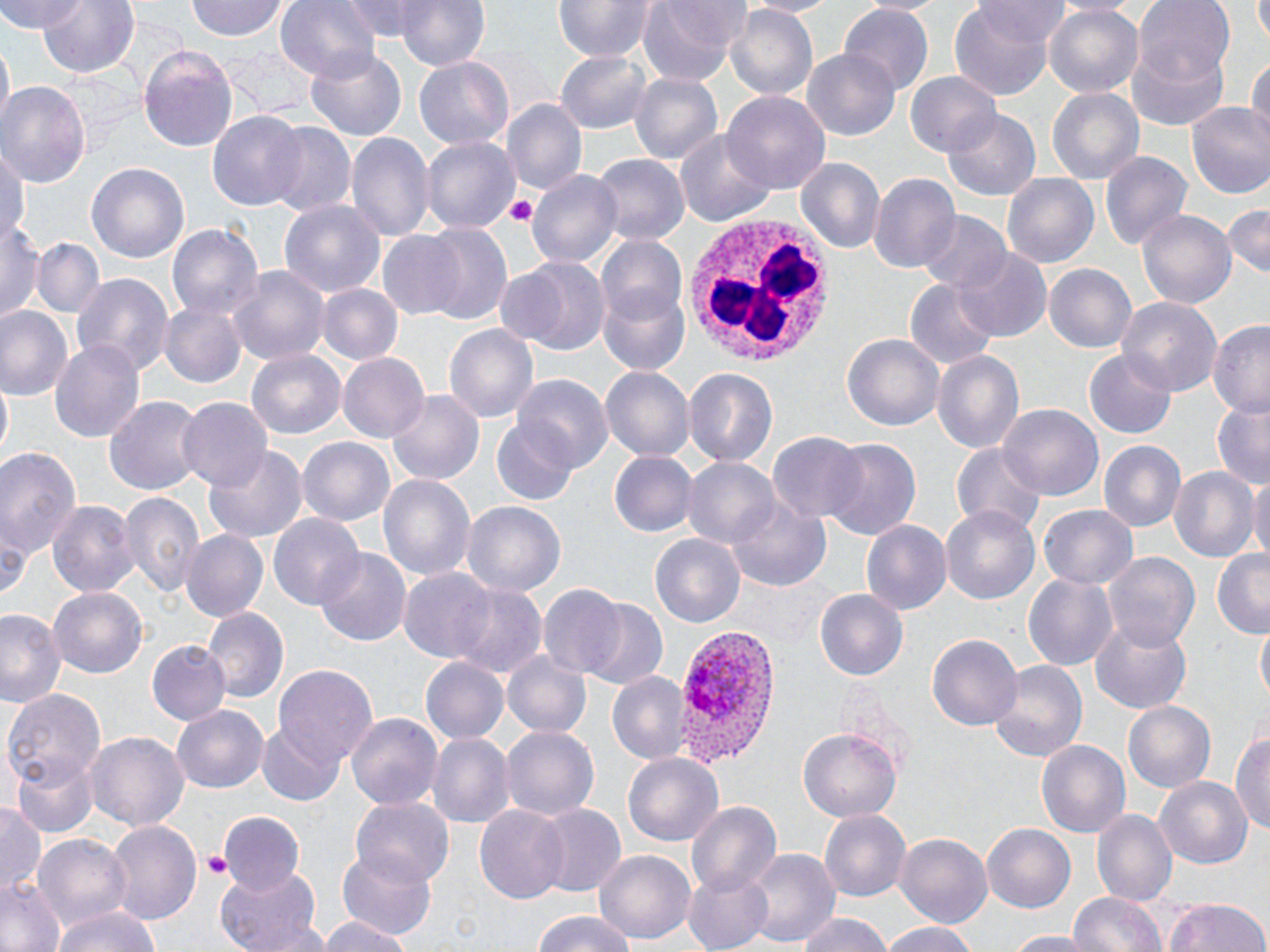

Summary:
  - Coordinate format: approximate bounding boxes as (x1,y1)-(x2,y2) corner pairs in pixels
  - Plasmodium vivax-infected red blood cell locations: (676,625)-(781,766)
  - White blood cell locations: (678,211)-(835,368)
  - Platelet locations: (501,194)-(539,225), (202,850)-(231,880)
  - Uninfected red blood cell locations: (3,0)-(82,34), (35,0)-(140,79), (186,0)-(289,41), (277,0)-(382,84), (341,0)-(436,39), (639,0)-(744,86), (742,0)-(839,18), (857,0)-(947,18), (971,0)-(1070,44), (1135,0)-(1235,87), (1254,0)-(1270,44), (390,1)-(492,69), (552,1)-(651,62), (1043,2)-(1145,99), (949,4)-(1060,99), (725,6)-(816,102), (841,7)-(933,93), (2,41)-(12,126), (1124,42)-(1230,130), (305,47)-(406,143), (555,48)-(654,136), (139,49)-(242,152), (800,50)-(901,141), (1249,56)-(1270,145), (415,57)-(514,152), (905,71)-(999,157), (629,72)-(722,169), (0,82)-(89,190), (1047,87)-(1145,187), (724,92)-(828,192), (503,99)-(586,199), (1185,102)-(1270,202), (208,110)-(310,210), (943,110)-(1041,202), (264,123)-(356,218), (676,130)-(774,226), (346,133)-(434,245), (421,137)-(518,235), (0,145)-(28,251), (1099,149)-(1193,253), (592,156)-(688,248), (795,159)-(884,253), (87,162)-(188,265), (529,170)-(623,270), (868,172)-(960,275), (1002,173)-(1099,269), (279,200)-(387,298), (1221,203)-(1270,280), (1137,207)-(1237,310), (919,211)-(1012,294), (3,217)-(45,323), (165,223)-(264,327), (420,224)-(513,327), (376,230)-(468,320), (594,237)-(689,328), (32,238)-(102,319), (954,247)-(1051,343), (512,258)-(611,355), (1042,263)-(1135,353), (229,265)-(329,368), (72,273)-(174,379), (906,277)-(999,371), (597,282)-(691,378), (316,284)-(402,366), (1115,296)-(1223,400), (158,298)-(246,390), (1,306)-(73,401), (1206,318)-(1270,418), (445,323)-(539,424), (842,334)-(944,432), (49,339)-(147,442), (246,350)-(345,440), (932,350)-(1025,456), (1085,352)-(1176,437), (339,355)-(427,442), (685,367)-(780,468), (600,368)-(694,461), (513,375)-(613,470), (1,383)-(11,461), (386,390)-(483,487), (105,394)-(203,495), (177,396)-(272,492), (1211,400)-(1269,488), (999,403)-(1102,502), (489,419)-(579,505), (768,431)-(868,526), (298,437)-(396,528), (820,439)-(921,541), (1099,441)-(1187,533), (950,443)-(1045,534), (0,444)-(83,562), (205,445)-(309,543), (609,453)-(694,535), (682,457)-(780,549), (1169,465)-(1259,565), (377,471)-(476,584), (1248,474)-(1270,566), (119,489)-(206,598), (50,499)-(138,600), (728,501)-(830,591), (462,502)-(565,600), (940,502)-(1040,602), (1038,505)-(1139,590), (268,512)-(364,611), (862,519)-(951,617), (181,530)-(267,621), (650,532)-(747,629), (315,548)-(412,647), (1104,551)-(1199,654), (1212,552)-(1270,637), (400,568)-(499,664), (1024,575)-(1117,669), (449,583)-(547,681), (537,585)-(625,679), (47,587)-(149,679), (813,588)-(910,682), (583,601)-(668,691), (201,606)-(289,704), (0,608)-(66,708), (1086,614)-(1195,718), (1257,623)-(1269,707), (927,632)-(1021,731), (147,642)-(230,727), (503,650)-(591,739), (421,658)-(509,745), (990,660)-(1086,764), (272,665)-(377,771), (607,673)-(692,766), (1,687)-(106,787), (1120,697)-(1216,792), (171,704)-(269,794), (347,713)-(443,811), (255,725)-(343,806), (501,725)-(597,824), (799,727)-(901,824), (1233,727)-(1270,841), (85,730)-(189,831), (425,731)-(512,828), (1037,739)-(1130,841), (623,752)-(723,849), (12,753)-(98,838), (1154,776)-(1252,873), (351,799)-(455,887), (687,800)-(783,898), (0,802)-(44,895), (533,803)-(626,900), (475,804)-(569,906), (1091,808)-(1177,907), (817,809)-(911,903), (217,813)-(306,896), (105,820)-(202,927), (982,824)-(1075,914), (895,833)-(991,930), (34,834)-(132,934), (338,847)-(437,941), (742,848)-(839,949), (594,850)-(694,947), (682,865)-(776,952), (217,867)-(324,952), (0,877)-(67,952), (1069,890)-(1168,952), (1165,897)-(1268,952), (49,906)-(163,952), (528,911)-(638,952), (791,913)-(898,952), (314,916)-(414,952), (878,920)-(982,952), (999,930)-(1102,950)
  - Slide-level diagnosis: Plasmodium vivax
  - Field of view: single
  - Magnification: 1000x
  - Preparation: thin blood film
  - Stain: May-Grünwald-Giemsa
  - Modality: optical microscopy
  - Image size: 1270×952 pixels